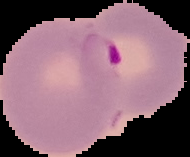
malaria status = parasitized
image size = 190×157 pixels
preparation = thin blood smear
image type = cell region segmented out of the field of view; surrounding area masked to black